Classify this cell by malaria status.
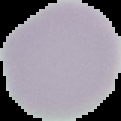

It is uninfected.

image type = segmented cell region with the area outside set to black
preparation = thin blood smear
image size = 121×121 pixels